Name the cell type shown.
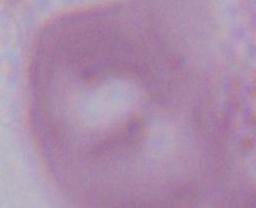
An erythrocyte.

{
  "modality": "photomicrograph",
  "magnification": "1000x"
}